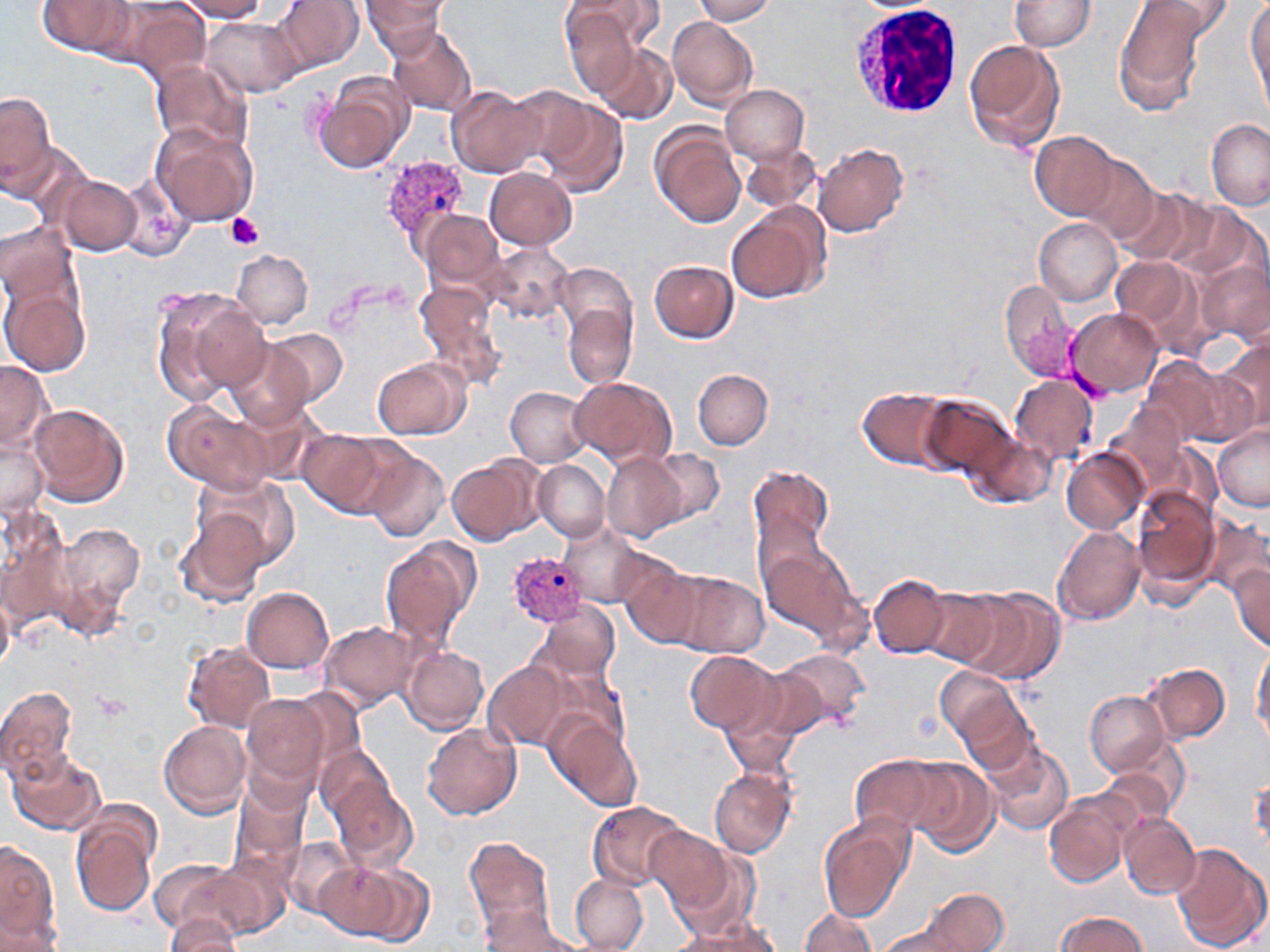

slide-level diagnosis = Plasmodium vivax
white blood cell locations = approximate bounding boxes as named x1/y1/x2/y2 corners in pixels: (x1=852, y1=1, x2=967, y2=119)
platelet locations = approximate bounding boxes as named x1/y1/x2/y2 corners in pixels: (x1=227, y1=213, x2=263, y2=250), (x1=92, y1=690, x2=131, y2=720)
stain = May-Grünwald-Giemsa
preparation = thin blood smear
magnification = 1000x
image size = 1270×952 pixels
Plasmodium vivax-infected red blood cell locations = approximate bounding boxes as named x1/y1/x2/y2 corners in pixels: (x1=381, y1=154, x2=471, y2=250), (x1=506, y1=548, x2=589, y2=630)
uninfected red blood cell locations = approximate bounding boxes as named x1/y1/x2/y2 corners in pixels: (x1=179, y1=0, x2=269, y2=21), (x1=274, y1=0, x2=362, y2=73), (x1=362, y1=0, x2=449, y2=55), (x1=694, y1=0, x2=776, y2=25), (x1=1007, y1=0, x2=1097, y2=52), (x1=1246, y1=0, x2=1269, y2=109), (x1=37, y1=1, x2=134, y2=56), (x1=571, y1=1, x2=664, y2=55), (x1=1113, y1=1, x2=1208, y2=117), (x1=1134, y1=1, x2=1235, y2=41), (x1=116, y1=3, x2=211, y2=81), (x1=560, y1=3, x2=648, y2=94), (x1=203, y1=17, x2=300, y2=97), (x1=667, y1=17, x2=758, y2=109), (x1=386, y1=24, x2=477, y2=116), (x1=963, y1=39, x2=1067, y2=152), (x1=593, y1=43, x2=677, y2=125), (x1=153, y1=60, x2=250, y2=148), (x1=313, y1=72, x2=413, y2=175), (x1=505, y1=83, x2=594, y2=170), (x1=721, y1=84, x2=809, y2=165), (x1=447, y1=87, x2=546, y2=178), (x1=1, y1=90, x2=55, y2=196), (x1=535, y1=95, x2=630, y2=198), (x1=1205, y1=119, x2=1270, y2=210), (x1=650, y1=121, x2=748, y2=228), (x1=151, y1=125, x2=257, y2=226), (x1=8, y1=129, x2=84, y2=218), (x1=1030, y1=129, x2=1119, y2=220), (x1=740, y1=139, x2=822, y2=216), (x1=813, y1=143, x2=910, y2=238), (x1=1072, y1=152, x2=1171, y2=247), (x1=486, y1=167, x2=577, y2=250), (x1=52, y1=174, x2=142, y2=258), (x1=1113, y1=185, x2=1215, y2=267), (x1=1166, y1=199, x2=1262, y2=285), (x1=726, y1=203, x2=829, y2=306), (x1=418, y1=210, x2=505, y2=293), (x1=1032, y1=216, x2=1122, y2=305), (x1=0, y1=220, x2=76, y2=308), (x1=481, y1=245, x2=575, y2=324), (x1=233, y1=249, x2=312, y2=328), (x1=1112, y1=254, x2=1195, y2=331), (x1=1198, y1=258, x2=1270, y2=346), (x1=649, y1=259, x2=738, y2=342), (x1=556, y1=277, x2=637, y2=390), (x1=1000, y1=279, x2=1075, y2=383), (x1=0, y1=280, x2=91, y2=377), (x1=414, y1=281, x2=508, y2=389), (x1=152, y1=286, x2=270, y2=404), (x1=1065, y1=307, x2=1162, y2=398), (x1=267, y1=328, x2=350, y2=405), (x1=224, y1=338, x2=314, y2=432), (x1=1214, y1=338, x2=1270, y2=440), (x1=1139, y1=357, x2=1240, y2=448), (x1=373, y1=358, x2=468, y2=440), (x1=0, y1=360, x2=51, y2=451), (x1=693, y1=369, x2=774, y2=449), (x1=570, y1=375, x2=678, y2=466), (x1=1011, y1=376, x2=1100, y2=463), (x1=505, y1=384, x2=591, y2=466), (x1=857, y1=387, x2=952, y2=469), (x1=916, y1=393, x2=1019, y2=480), (x1=163, y1=401, x2=274, y2=491), (x1=29, y1=402, x2=131, y2=508), (x1=1107, y1=403, x2=1196, y2=497), (x1=1, y1=415, x2=50, y2=519), (x1=1212, y1=424, x2=1270, y2=510), (x1=299, y1=429, x2=407, y2=519), (x1=964, y1=429, x2=1057, y2=510), (x1=1062, y1=448, x2=1147, y2=533), (x1=361, y1=449, x2=449, y2=543), (x1=644, y1=449, x2=725, y2=528), (x1=602, y1=451, x2=690, y2=540), (x1=446, y1=455, x2=540, y2=544), (x1=533, y1=459, x2=608, y2=542), (x1=749, y1=463, x2=836, y2=559), (x1=191, y1=473, x2=301, y2=572), (x1=1132, y1=485, x2=1221, y2=597), (x1=0, y1=503, x2=73, y2=633), (x1=1201, y1=508, x2=1269, y2=597), (x1=177, y1=510, x2=270, y2=607), (x1=556, y1=517, x2=649, y2=608), (x1=50, y1=520, x2=145, y2=633), (x1=1053, y1=525, x2=1146, y2=625), (x1=757, y1=532, x2=873, y2=649), (x1=380, y1=536, x2=480, y2=652), (x1=623, y1=563, x2=707, y2=648), (x1=1227, y1=563, x2=1270, y2=651), (x1=669, y1=569, x2=771, y2=657), (x1=870, y1=573, x2=953, y2=657), (x1=0, y1=581, x2=15, y2=675), (x1=919, y1=583, x2=1013, y2=668), (x1=956, y1=585, x2=1064, y2=684), (x1=241, y1=586, x2=335, y2=673), (x1=539, y1=603, x2=622, y2=683), (x1=320, y1=620, x2=422, y2=710), (x1=183, y1=641, x2=274, y2=732), (x1=1251, y1=644, x2=1269, y2=739), (x1=403, y1=645, x2=489, y2=734), (x1=768, y1=647, x2=871, y2=737), (x1=685, y1=650, x2=778, y2=733), (x1=482, y1=659, x2=575, y2=751), (x1=1143, y1=661, x2=1230, y2=742), (x1=936, y1=666, x2=1025, y2=754), (x1=719, y1=671, x2=823, y2=767), (x1=0, y1=685, x2=80, y2=784), (x1=1086, y1=689, x2=1168, y2=775), (x1=240, y1=691, x2=331, y2=797), (x1=955, y1=692, x2=1040, y2=777), (x1=548, y1=713, x2=642, y2=812), (x1=158, y1=720, x2=252, y2=818), (x1=422, y1=723, x2=522, y2=819), (x1=990, y1=741, x2=1074, y2=834), (x1=1100, y1=741, x2=1189, y2=824), (x1=314, y1=745, x2=400, y2=839), (x1=7, y1=747, x2=108, y2=837), (x1=849, y1=753, x2=965, y2=839), (x1=908, y1=759, x2=1000, y2=858), (x1=708, y1=765, x2=796, y2=857), (x1=331, y1=771, x2=418, y2=870), (x1=1248, y1=774, x2=1269, y2=849), (x1=230, y1=778, x2=310, y2=879), (x1=1044, y1=795, x2=1133, y2=888), (x1=587, y1=800, x2=691, y2=892), (x1=71, y1=808, x2=158, y2=917), (x1=1121, y1=813, x2=1199, y2=899), (x1=817, y1=815, x2=913, y2=919), (x1=645, y1=825, x2=735, y2=923), (x1=281, y1=835, x2=358, y2=920), (x1=464, y1=835, x2=553, y2=938), (x1=0, y1=840, x2=58, y2=946), (x1=1172, y1=843, x2=1269, y2=952), (x1=207, y1=853, x2=295, y2=941), (x1=152, y1=856, x2=250, y2=940), (x1=315, y1=858, x2=424, y2=944), (x1=570, y1=875, x2=650, y2=952), (x1=923, y1=887, x2=1010, y2=950), (x1=473, y1=905, x2=589, y2=951), (x1=800, y1=908, x2=876, y2=951), (x1=1056, y1=912, x2=1148, y2=952), (x1=160, y1=914, x2=243, y2=951), (x1=675, y1=914, x2=784, y2=952), (x1=869, y1=914, x2=984, y2=951)
modality = light microscopy
field of view = single